Comment on the morphology of the erythrocytes.
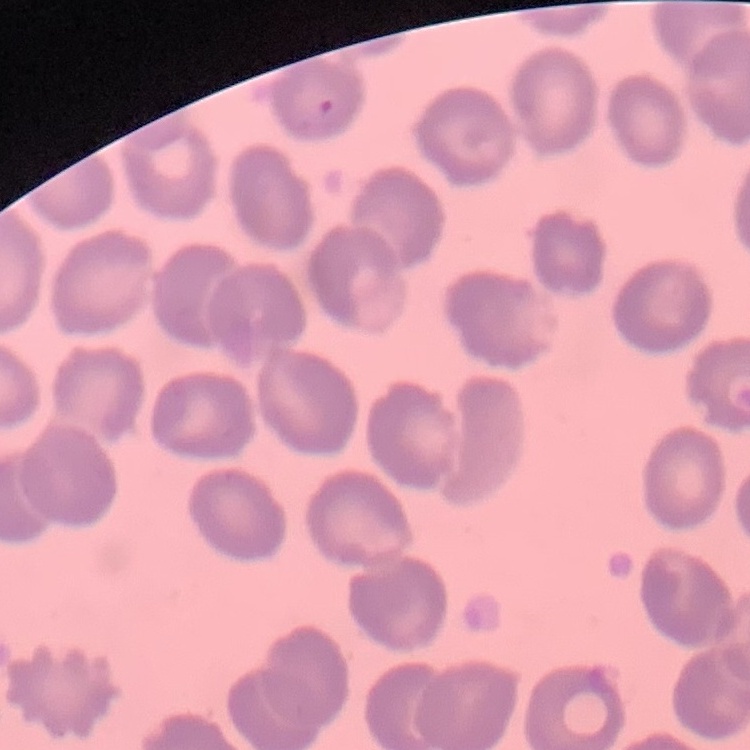
They show no rouleaux formation.

preparation = thin blood smear
stain = Field's or Giemsa
image type = square crop of a larger photomicrograph